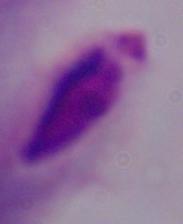
magnification = 1000x
modality = micrograph
identification = trichomonad